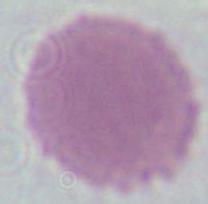
modality = photomicrograph
magnification = 1000x
identification = red blood cell